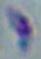
Summary:
  - Identification: Toxoplasma gondii
  - Magnification: 1000x
  - Modality: micrograph